Identify the cell.
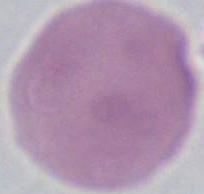

An erythrocyte.

magnification = 1000x
modality = photomicrograph